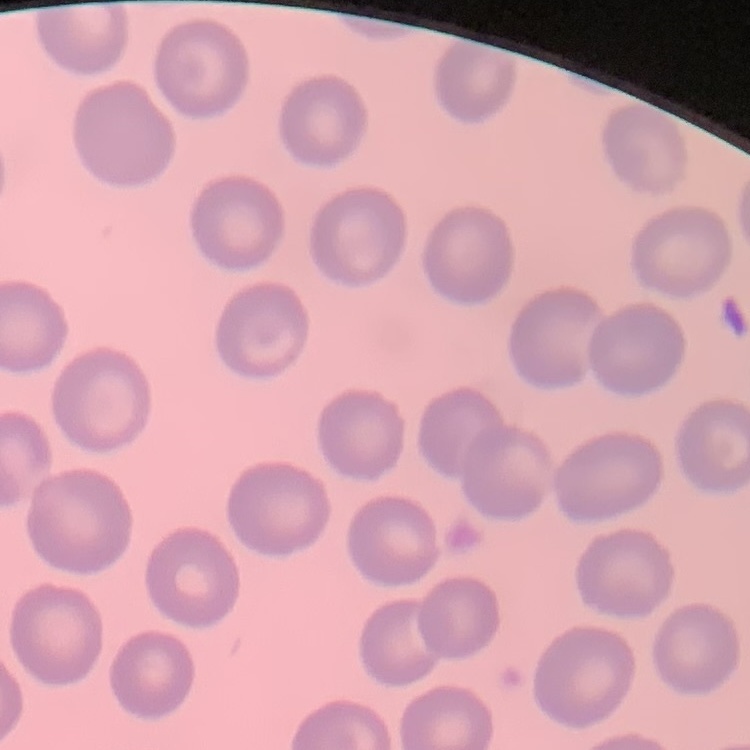
Summary:
  - Red blood cell morphology: no rouleaux formation
  - Preparation: thin blood film
  - Stain: Field's or Giemsa
  - Image type: square crop of a larger photomicrograph